Comment on the morphology of the erythrocytes.
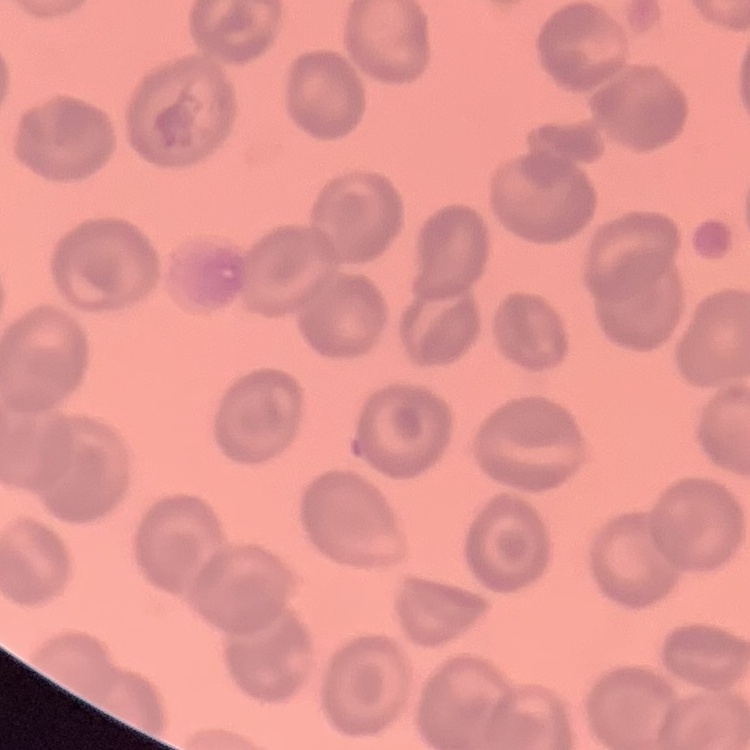

No rouleaux formation.

image type = one tile cut from a larger photomicrograph
stain = Field's or Giemsa
preparation = thin blood film